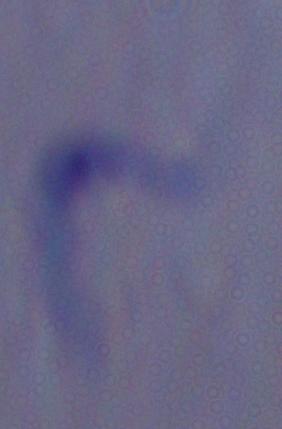
Summary:
  - Modality: photomicrograph
  - Identification: trypanosome
  - Magnification: 1000x